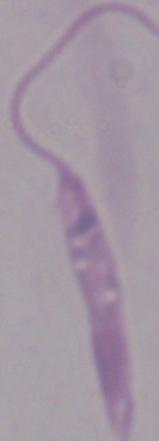

Summary:
  - Modality: micrograph
  - Magnification: 1000x
  - Identification: Leishmania